Locate platelets.
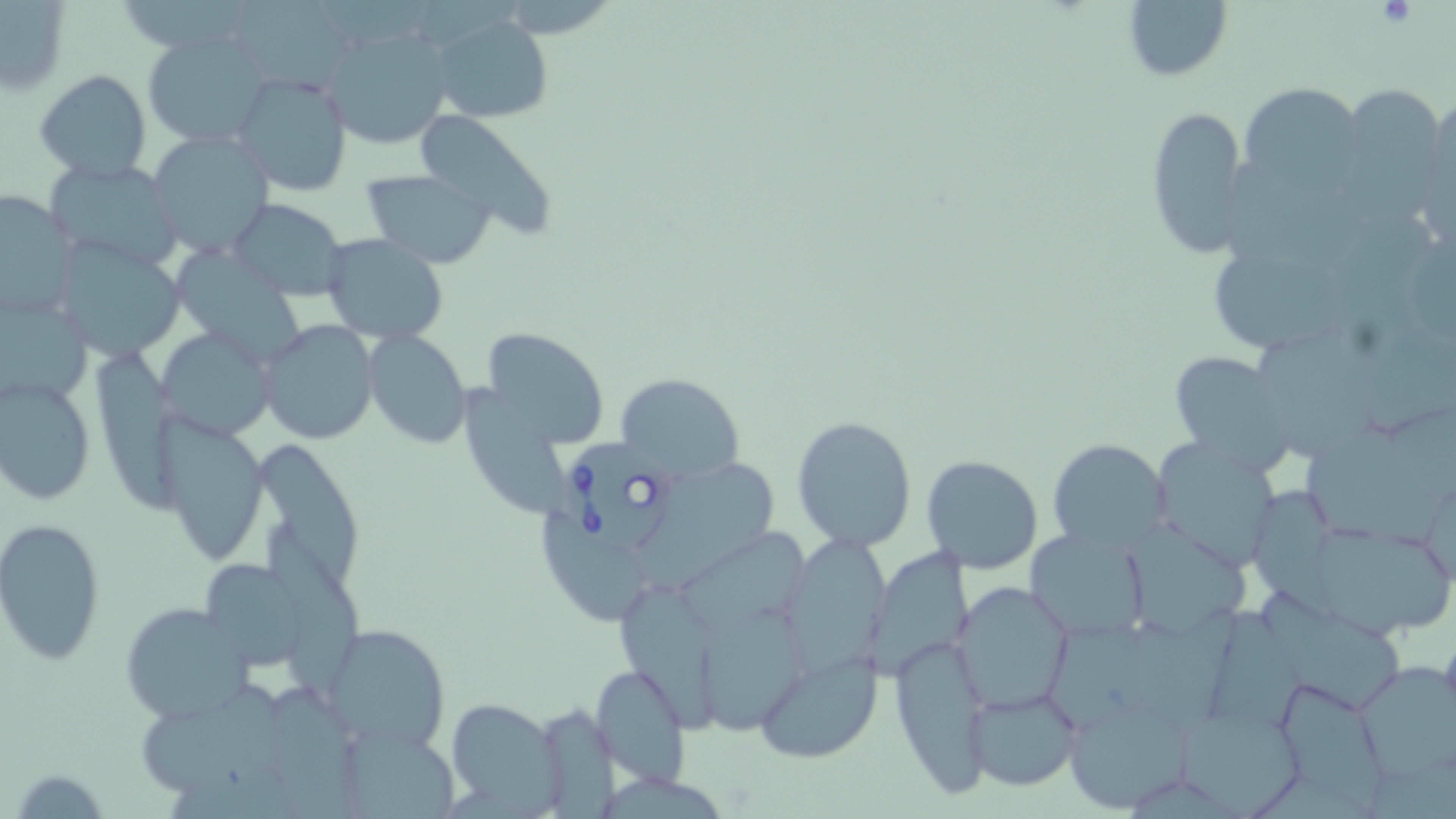
Approximate bounding boxes as [x1, y1, x2, y2] in pixels.
Platelets: [1378, 0, 1419, 29].

Summary:
  - Babesia divergens-infected red blood cell locations: [560, 434, 671, 559]
  - Uninfected red blood cell locations: [228, 0, 354, 91], [1121, 0, 1232, 84], [0, 2, 70, 96], [431, 13, 552, 123], [325, 28, 455, 154], [143, 32, 273, 148], [34, 70, 152, 182], [231, 70, 353, 197], [1235, 81, 1365, 192], [1336, 82, 1449, 211], [1425, 97, 1456, 212], [1144, 103, 1249, 259], [414, 110, 556, 235], [147, 131, 276, 259], [44, 158, 186, 270], [360, 168, 496, 267], [0, 188, 80, 324], [227, 198, 348, 300], [1334, 213, 1436, 349], [322, 234, 449, 344], [55, 238, 187, 360], [178, 241, 314, 366], [1212, 254, 1347, 365], [0, 294, 91, 409], [260, 320, 378, 445], [481, 320, 606, 446], [154, 327, 278, 442], [361, 329, 471, 448], [1258, 331, 1387, 458], [100, 353, 190, 515], [1171, 353, 1294, 468], [613, 372, 745, 484], [1, 376, 96, 506], [458, 385, 573, 518], [792, 414, 917, 551], [157, 416, 269, 565], [1304, 426, 1443, 547], [1045, 438, 1170, 553], [1153, 439, 1279, 565], [266, 447, 362, 590], [921, 455, 1045, 574], [645, 458, 782, 590], [1252, 482, 1347, 618], [543, 513, 654, 621], [0, 518, 107, 666], [1129, 521, 1249, 637], [1321, 524, 1454, 634], [270, 526, 363, 702], [1025, 527, 1151, 642], [682, 534, 813, 626], [782, 538, 890, 675], [197, 556, 313, 671], [951, 581, 1076, 714], [620, 583, 725, 738], [1260, 591, 1402, 715], [119, 600, 254, 725], [701, 601, 809, 731], [1211, 606, 1299, 743], [327, 624, 450, 752], [888, 634, 993, 795], [754, 650, 882, 763], [1355, 663, 1456, 783], [591, 664, 692, 786], [1268, 678, 1390, 807], [963, 686, 1083, 793], [141, 687, 293, 796], [1063, 691, 1196, 814], [447, 698, 564, 814], [540, 701, 620, 819], [1179, 709, 1308, 818], [335, 722, 460, 819], [7, 766, 113, 817]
  - Slide-level diagnosis: Babesia divergens
  - Magnification: 1000x
  - Stain: May-Grünwald-Giemsa
  - Image size: 1456×819 pixels
  - Modality: optical microscopy
  - Field of view: one of a larger specimen
  - Preparation: thin blood film